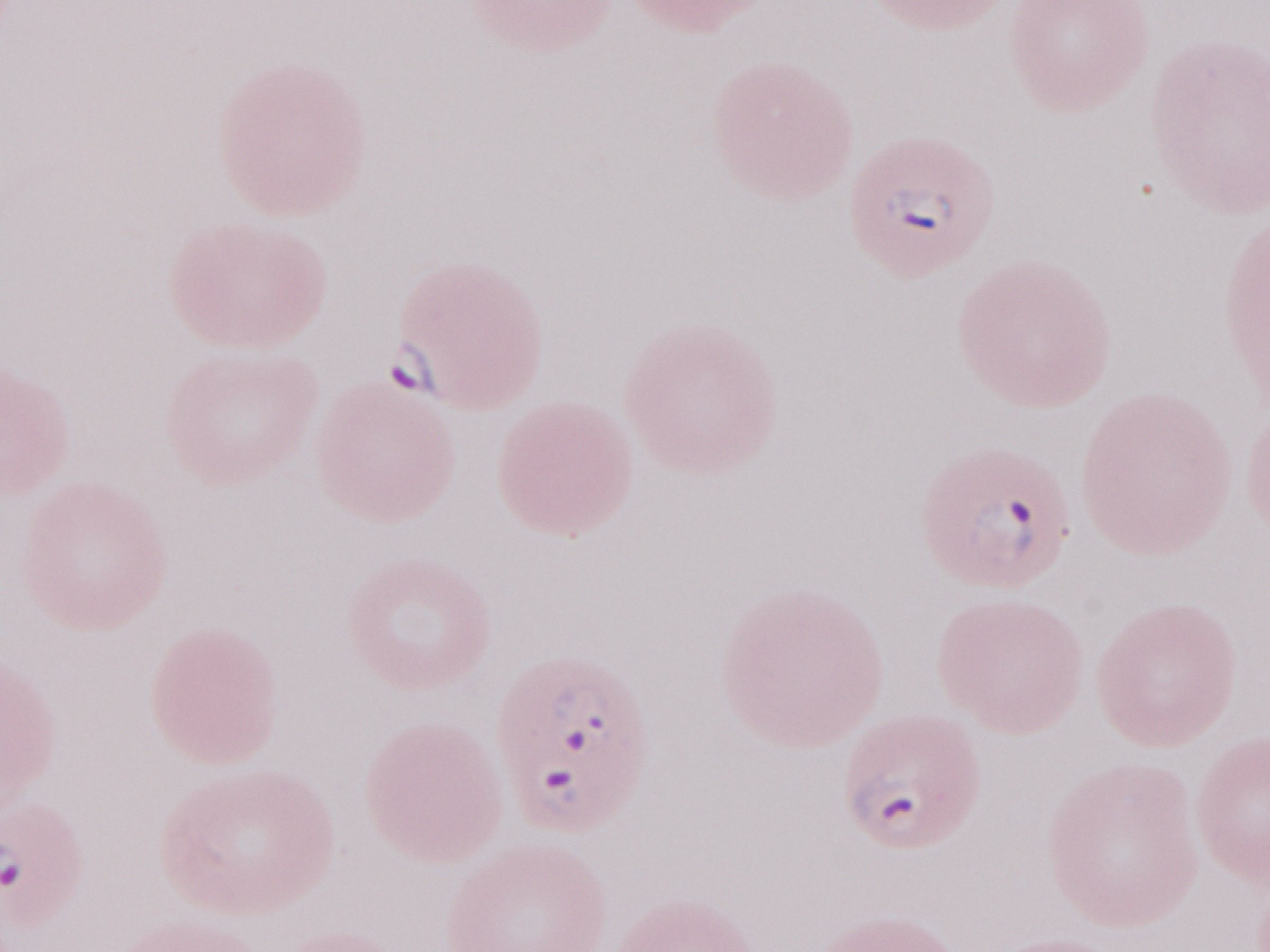 Patient-level malaria diagnosis: positive. Single field of view. Thin peripheral-blood smear. Image is 1270×952 pixels. May-Grünwald-Giemsa stain. Magnification: 1,000x. Olympus BX43 microscope and DP73 digital camera.